Name the blood parasite species.
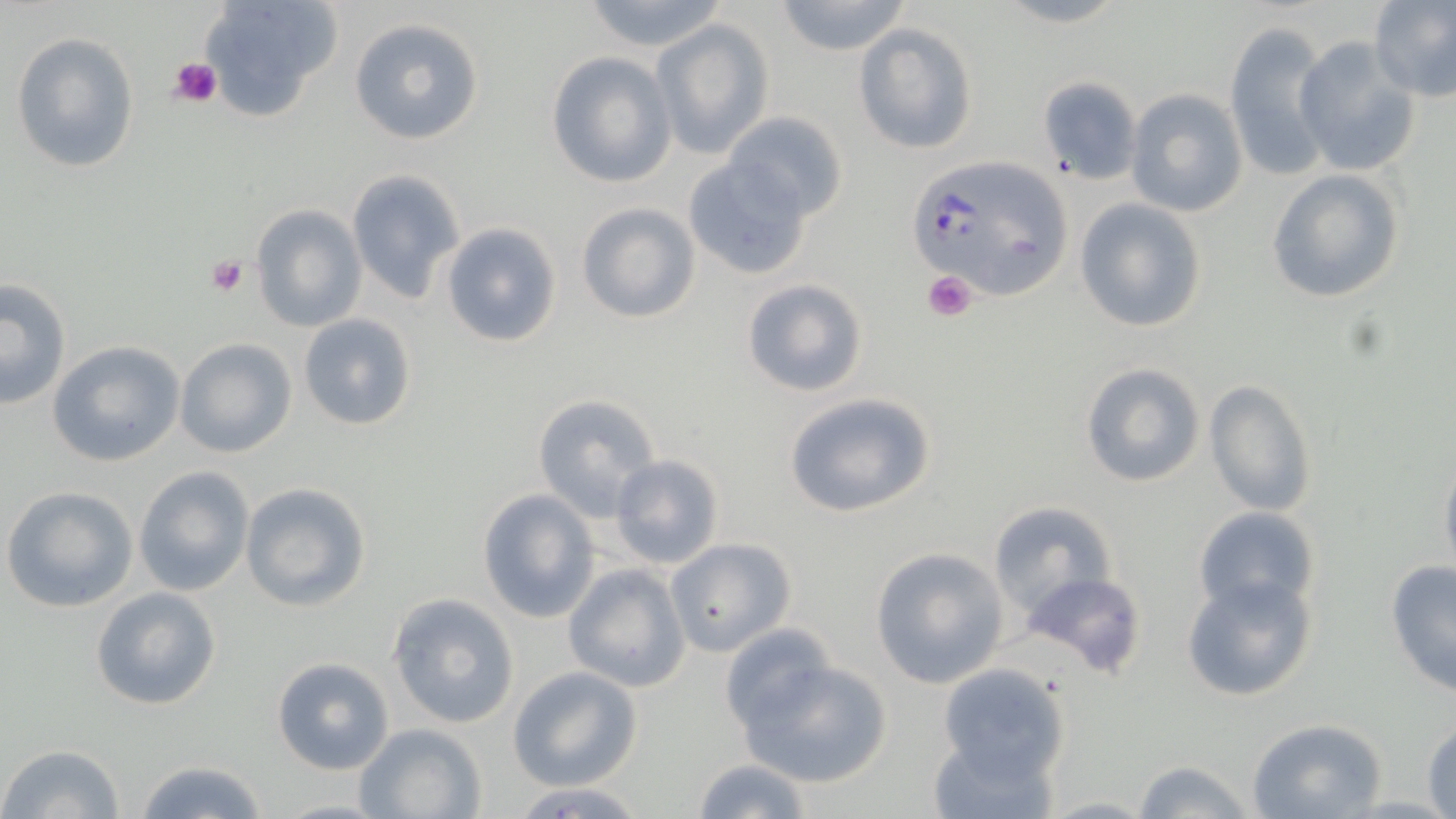

Plasmodium falciparum.

Summary:
  - Coordinate format: approximate bounding boxes as named x1/y1/x2/y2 corners in pixels
  - Platelet locations: (x1=166, y1=55, x2=223, y2=111), (x1=206, y1=255, x2=249, y2=298), (x1=923, y1=270, x2=977, y2=322)
  - Plasmodium falciparum-infected red blood cell locations: (x1=904, y1=154, x2=1072, y2=300)
  - Uninfected red blood cell locations: (x1=198, y1=0, x2=342, y2=117), (x1=578, y1=0, x2=730, y2=51), (x1=772, y1=0, x2=912, y2=56), (x1=1368, y1=0, x2=1456, y2=103), (x1=349, y1=18, x2=484, y2=145), (x1=652, y1=18, x2=775, y2=160), (x1=1223, y1=18, x2=1335, y2=183), (x1=853, y1=24, x2=977, y2=155), (x1=10, y1=31, x2=141, y2=173), (x1=1293, y1=37, x2=1422, y2=177), (x1=546, y1=51, x2=676, y2=188), (x1=1035, y1=75, x2=1143, y2=184), (x1=1126, y1=89, x2=1248, y2=217), (x1=724, y1=111, x2=849, y2=223), (x1=683, y1=157, x2=813, y2=280), (x1=346, y1=168, x2=466, y2=304), (x1=1266, y1=169, x2=1404, y2=303), (x1=1075, y1=199, x2=1206, y2=332), (x1=575, y1=202, x2=701, y2=323), (x1=251, y1=204, x2=366, y2=332), (x1=441, y1=222, x2=563, y2=348), (x1=0, y1=278, x2=72, y2=410), (x1=740, y1=278, x2=868, y2=396), (x1=297, y1=312, x2=418, y2=432), (x1=174, y1=338, x2=297, y2=458), (x1=48, y1=340, x2=186, y2=466), (x1=1080, y1=361, x2=1205, y2=488), (x1=1203, y1=378, x2=1318, y2=517), (x1=785, y1=391, x2=936, y2=518), (x1=532, y1=393, x2=660, y2=519), (x1=1439, y1=452, x2=1456, y2=584), (x1=610, y1=453, x2=723, y2=568), (x1=134, y1=467, x2=253, y2=596), (x1=240, y1=482, x2=371, y2=610), (x1=1, y1=485, x2=139, y2=613), (x1=477, y1=489, x2=601, y2=623), (x1=987, y1=502, x2=1119, y2=621), (x1=1194, y1=506, x2=1320, y2=618), (x1=666, y1=537, x2=795, y2=658), (x1=869, y1=546, x2=1008, y2=689), (x1=1383, y1=562, x2=1456, y2=695), (x1=562, y1=563, x2=691, y2=692), (x1=1019, y1=569, x2=1151, y2=683), (x1=1181, y1=572, x2=1320, y2=702), (x1=90, y1=586, x2=222, y2=712), (x1=388, y1=593, x2=520, y2=729), (x1=719, y1=623, x2=838, y2=738), (x1=732, y1=654, x2=894, y2=789), (x1=271, y1=656, x2=395, y2=775), (x1=938, y1=662, x2=1069, y2=780), (x1=507, y1=665, x2=642, y2=790), (x1=1246, y1=717, x2=1389, y2=818), (x1=1423, y1=718, x2=1456, y2=817), (x1=354, y1=723, x2=486, y2=819), (x1=927, y1=730, x2=1059, y2=819), (x1=2, y1=743, x2=125, y2=819), (x1=133, y1=757, x2=268, y2=819), (x1=691, y1=758, x2=813, y2=818), (x1=1131, y1=758, x2=1256, y2=818), (x1=505, y1=782, x2=652, y2=818), (x1=274, y1=798, x2=392, y2=818)
  - Preparation: thin blood smear
  - Field of view: one of a larger specimen
  - Modality: light microscopy
  - Stain: May-Grünwald-Giemsa
  - Image size: 1456×819 pixels
  - Magnification: 1000x